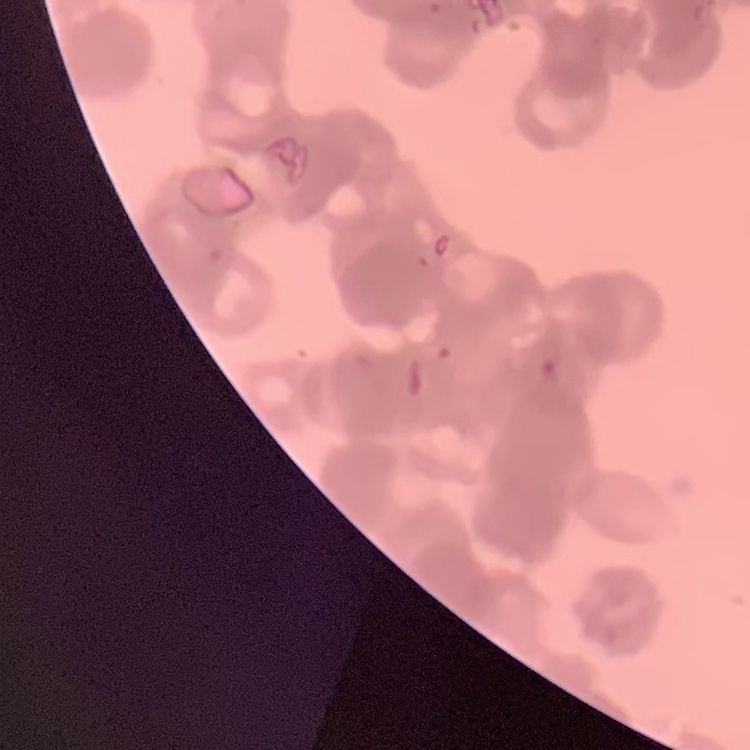 The erythrocytes show rouleaux formation. Thin peripheral smear. Stained with either Field's or Giemsa. Square crop of a larger photomicrograph.